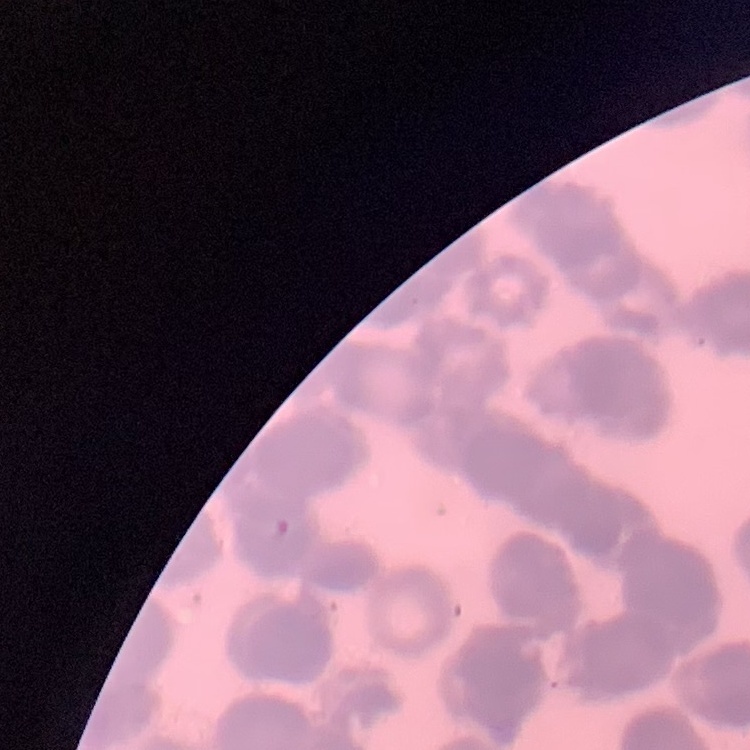

Summary:
  - Erythrocyte morphology: rouleaux formation
  - Preparation: thin blood film
  - Image type: square crop of a larger photomicrograph
  - Stain: Field's or Giemsa